Classify this cell by malaria status.
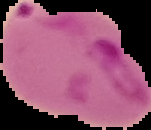
It is parasitized.

{
  "image_type": "segmented cell region with the area outside set to black",
  "image_size": "151×130 pixels",
  "preparation": "thin blood film"
}